Evaluate for Plasmodium parasites.
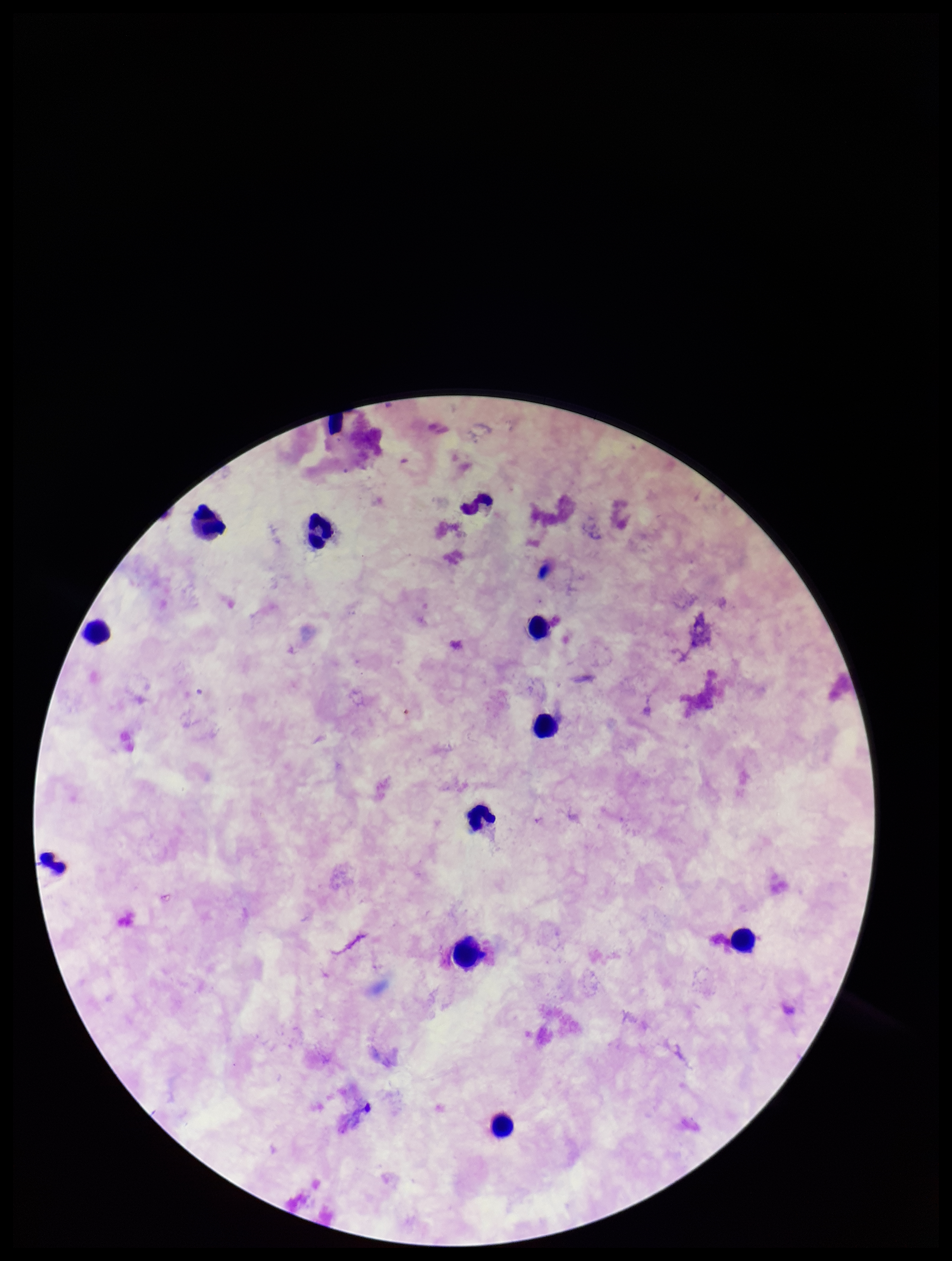

None seen.

Parasite count: 0. One field from this slide. Patient malaria status: negative. Leukocyte count: 9. Preparation: thick. Image is 952×1261 pixels. Smartphone photograph taken through the eyepiece of a microscope. Stained with Giemsa.